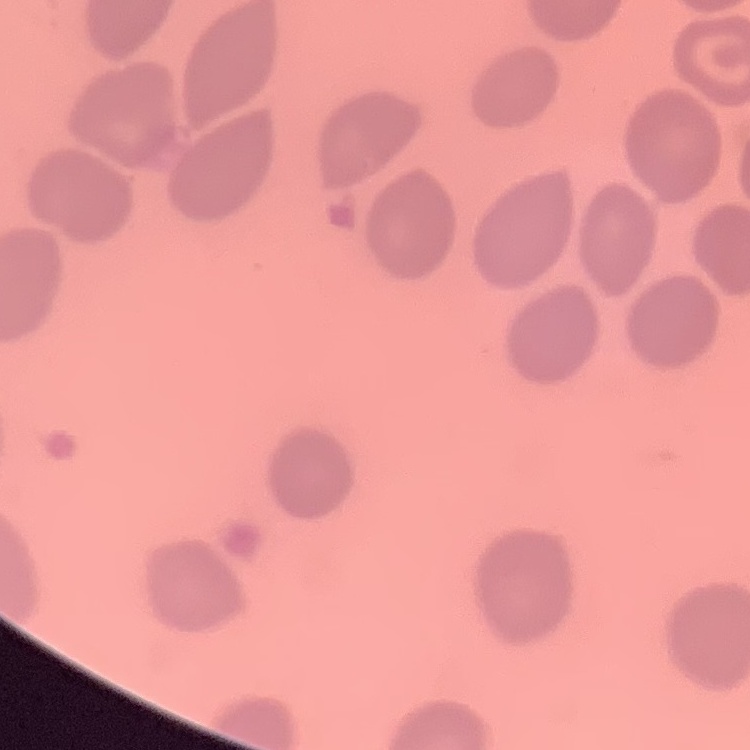

erythrocyte_morphology: no rouleaux formation
preparation: thin blood film
image_type: one tile cut from a larger photomicrograph
stain: Field's or Giemsa